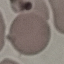
malaria_status: uninfected
capture: smartphone camera at the microscope eyepiece
preparation: thin smear
image_type: automatically extracted cell patch, resized to 64 × 64 pixels
stain: Giemsa